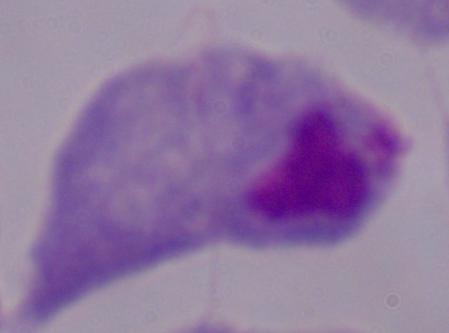 A trichomonad is seen. 1000x magnification. Micrograph.